Give a bounding box for every malaria parasite.
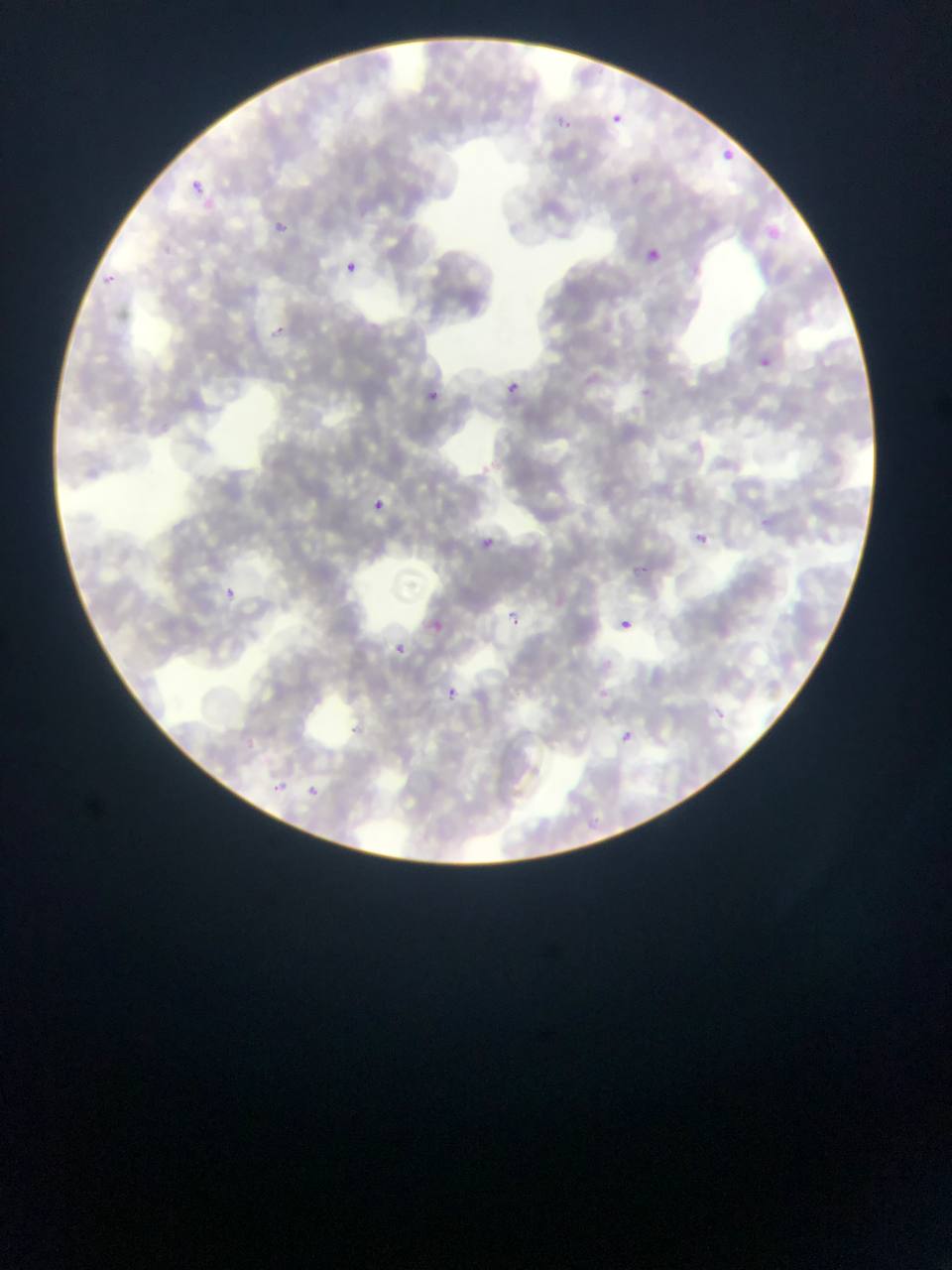
Approximate bounding boxes as {left, top, right, bottom} in pixels.
Malaria parasites: {610, 109, 633, 132}, {555, 119, 572, 135}, {719, 148, 740, 163}, {188, 180, 208, 200}, {276, 221, 294, 233}, {767, 228, 783, 244}, {643, 248, 658, 261}, {344, 259, 358, 276}, {267, 325, 284, 337}, {760, 356, 774, 370}, {502, 380, 524, 392}, {424, 389, 444, 403}, {371, 497, 388, 509}, {694, 531, 710, 546}, {481, 535, 501, 551}, {224, 584, 242, 599}, {507, 613, 526, 626}, {433, 618, 451, 634}, {621, 619, 631, 630}, {392, 640, 410, 651}, {448, 685, 461, 702}, {597, 686, 617, 701}, {619, 731, 631, 744}, {265, 778, 283, 792}, {308, 784, 320, 798}.

Summary:
  - Country: Ghana
  - Capture: mobile-phone photograph through a microscope
  - Image size: 952×1270 pixels
  - Field of view: single
  - Preparation: thin blood smear